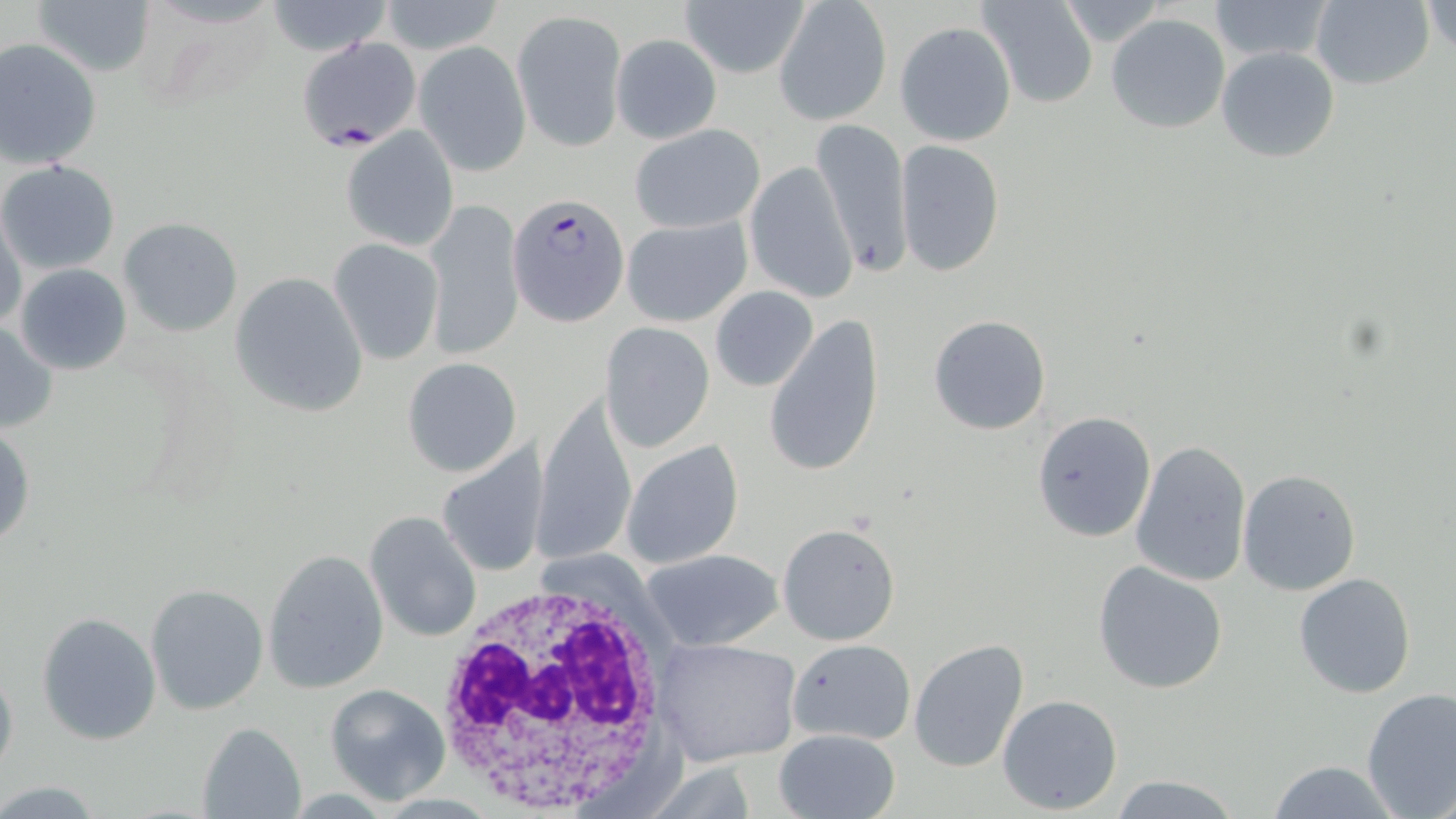

Approximate bounding boxes as named x1/y1/x2/y2 corners in pixels. White blood cell locations: (x1=433, y1=575, x2=678, y2=810). Uninfected red blood cell locations: (x1=678, y1=0, x2=809, y2=79), (x1=978, y1=0, x2=1099, y2=109), (x1=1205, y1=0, x2=1335, y2=64), (x1=1310, y1=0, x2=1436, y2=90), (x1=30, y1=1, x2=154, y2=76), (x1=263, y1=1, x2=395, y2=56), (x1=378, y1=1, x2=507, y2=58), (x1=1424, y1=1, x2=1455, y2=55), (x1=774, y1=2, x2=891, y2=126), (x1=1048, y1=2, x2=1175, y2=45), (x1=513, y1=9, x2=626, y2=152), (x1=1106, y1=12, x2=1231, y2=134), (x1=895, y1=20, x2=1017, y2=147), (x1=611, y1=34, x2=722, y2=143), (x1=0, y1=38, x2=103, y2=170), (x1=415, y1=40, x2=531, y2=176), (x1=1216, y1=46, x2=1341, y2=163), (x1=811, y1=117, x2=911, y2=279), (x1=630, y1=123, x2=764, y2=234), (x1=340, y1=125, x2=459, y2=253), (x1=895, y1=140, x2=1006, y2=277), (x1=0, y1=160, x2=121, y2=275), (x1=744, y1=161, x2=858, y2=304), (x1=421, y1=198, x2=525, y2=361), (x1=1, y1=211, x2=29, y2=334), (x1=621, y1=216, x2=751, y2=326), (x1=118, y1=217, x2=244, y2=338), (x1=329, y1=238, x2=444, y2=365), (x1=14, y1=263, x2=132, y2=376), (x1=230, y1=272, x2=368, y2=418), (x1=710, y1=286, x2=819, y2=392), (x1=928, y1=314, x2=1052, y2=435), (x1=765, y1=315, x2=885, y2=480), (x1=0, y1=319, x2=57, y2=434), (x1=601, y1=322, x2=715, y2=452), (x1=402, y1=357, x2=522, y2=476), (x1=533, y1=394, x2=636, y2=566), (x1=1030, y1=410, x2=1156, y2=544), (x1=0, y1=424, x2=34, y2=552), (x1=624, y1=440, x2=743, y2=569), (x1=1130, y1=440, x2=1251, y2=587), (x1=436, y1=442, x2=549, y2=579), (x1=1237, y1=470, x2=1362, y2=595), (x1=364, y1=509, x2=483, y2=644), (x1=776, y1=523, x2=901, y2=647), (x1=261, y1=547, x2=388, y2=694), (x1=640, y1=549, x2=783, y2=651), (x1=1091, y1=559, x2=1230, y2=695), (x1=1293, y1=571, x2=1417, y2=698), (x1=145, y1=583, x2=270, y2=716), (x1=36, y1=612, x2=161, y2=745), (x1=652, y1=636, x2=801, y2=768), (x1=790, y1=637, x2=914, y2=743), (x1=909, y1=638, x2=1030, y2=772), (x1=0, y1=661, x2=18, y2=781), (x1=324, y1=683, x2=450, y2=803), (x1=1358, y1=687, x2=1456, y2=817), (x1=997, y1=693, x2=1123, y2=814), (x1=195, y1=721, x2=306, y2=819), (x1=775, y1=729, x2=900, y2=817), (x1=1262, y1=760, x2=1404, y2=819), (x1=1109, y1=774, x2=1241, y2=818), (x1=0, y1=780, x2=104, y2=814). Plasmodium falciparum-infected red blood cell locations: (x1=299, y1=38, x2=422, y2=151), (x1=511, y1=192, x2=629, y2=321). Slide-level diagnosis: Plasmodium falciparum. 1000x magnification. Thin blood film. Image is 1456×819 pixels. Single field of view. May-Grünwald-Giemsa-stained preparation. Light microscopy.